Locate every malaria parasite and every leukocyte.
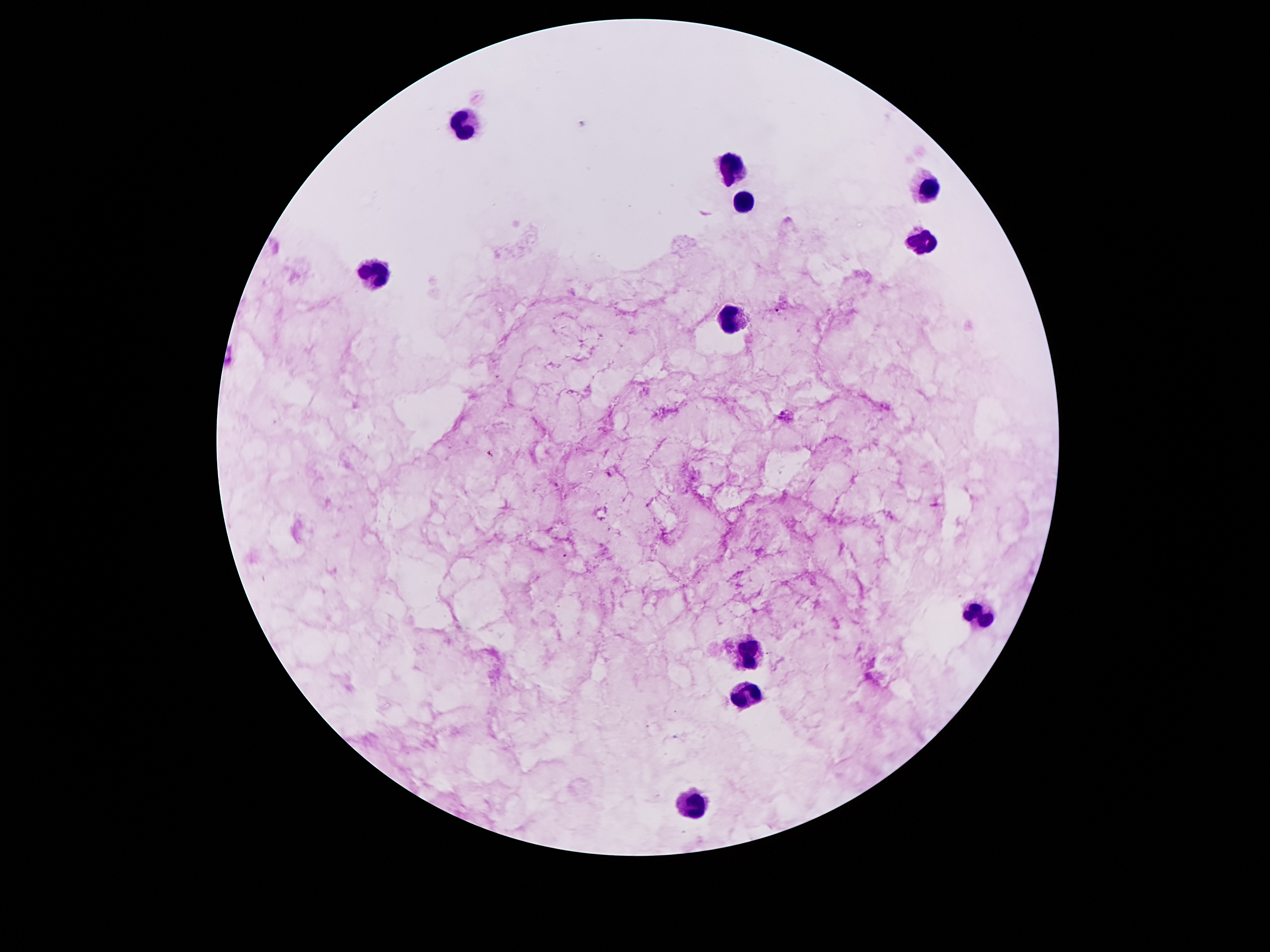
Approximate centers as [x, y] in pixels.
Malaria parasites: [776, 311], [490, 453], [567, 555].
Leukocytes: [464, 121], [733, 167], [928, 189], [742, 200], [921, 240], [377, 275], [731, 315], [983, 615], [749, 659], [749, 696], [694, 805].

patient malaria status = positive for Plasmodium falciparum
image size = 1270×952 pixels
capture = smartphone through the microscope eyepiece
stain = Giemsa
magnification = 100x
preparation = thick blood smear
field of view = single